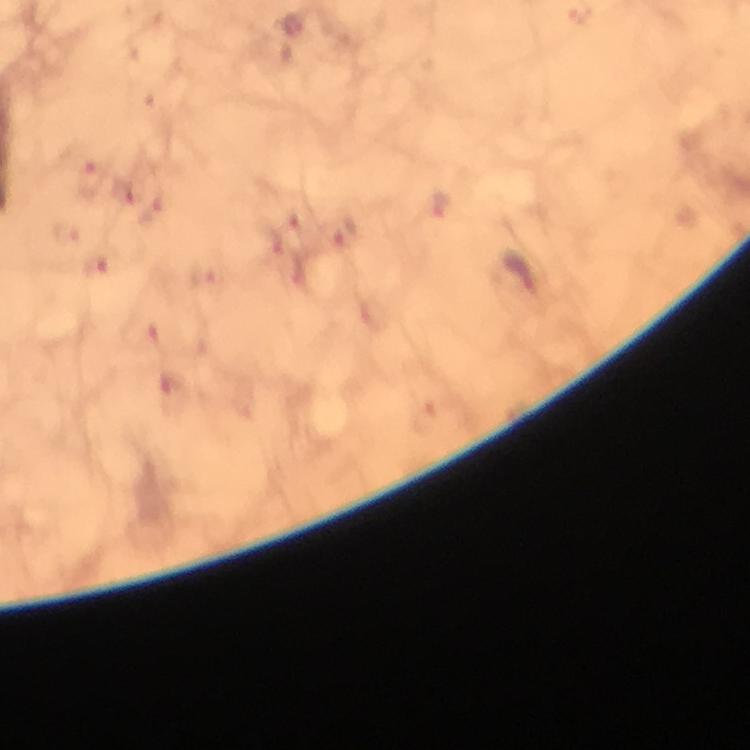

{
  "plasmodium_parasite_locations": "approximate centers as (x, y) in pixels: (293, 26), (92, 181), (124, 192), (346, 230), (67, 234), (273, 243), (96, 266), (524, 274), (201, 275), (171, 388)",
  "stain": "Giemsa",
  "immersion_oil": "used",
  "context": "from a diagnostic examination for malaria",
  "preparation": "thick smear",
  "image_size": "750×750 pixels",
  "cropped_from": "a single field of view",
  "magnification": "100x",
  "capture": "smartphone camera through the microscope"
}